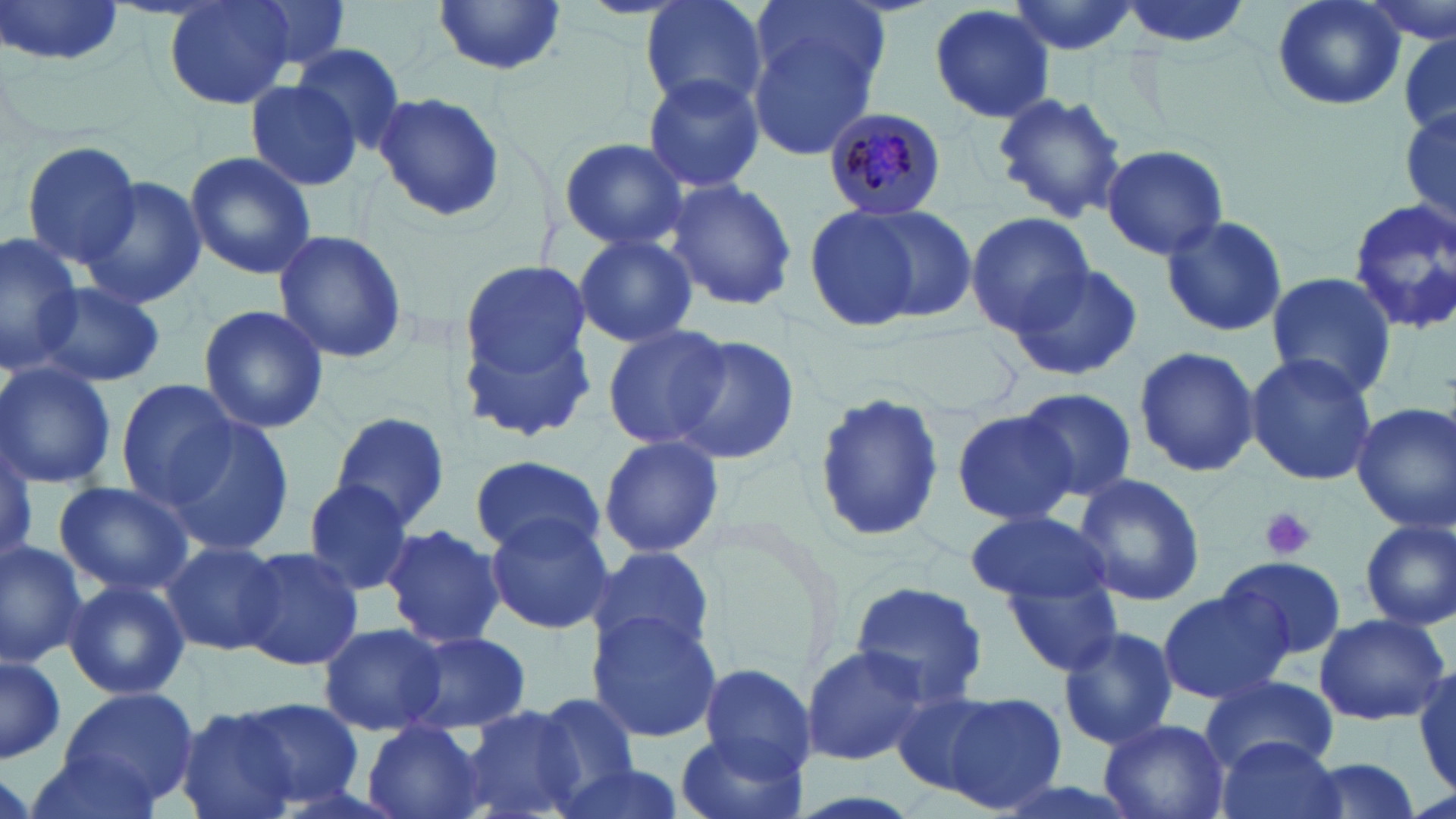
Plasmodium malariae-infected red blood cell locations = approximate bounding boxes as (x1,y1)-(x2,y2) corner pairs in pixels: (821,104)-(951,215)
slide-level diagnosis = Plasmodium malariae
stain = May-Grünwald-Giemsa
platelet locations = approximate bounding boxes as (x1,y1)-(x2,y2) corner pairs in pixels: (1257,506)-(1318,561)
magnification = 1000x
modality = optical microscopy
preparation = thin blood film
uninfected red blood cell locations = approximate bounding boxes as (x1,y1)-(x2,y2) corner pairs in pixels: (162,0)-(295,110), (241,0)-(353,74), (639,0)-(769,115), (751,0)-(893,95), (1003,0)-(1140,57), (1113,0)-(1255,52), (1271,0)-(1405,112), (1362,0)-(1456,47), (1,1)-(127,69), (432,2)-(568,77), (927,4)-(1057,125), (743,20)-(883,162), (1399,38)-(1455,136), (287,43)-(407,152), (641,71)-(766,194), (242,79)-(363,191), (990,90)-(1128,224), (371,92)-(506,222), (1400,96)-(1454,241), (556,137)-(692,253), (19,139)-(145,268), (1100,144)-(1229,260), (183,151)-(316,279), (79,176)-(208,308), (661,177)-(798,311), (1347,199)-(1456,335), (802,203)-(931,335), (846,204)-(978,322), (964,211)-(1096,339), (1160,214)-(1287,338), (272,230)-(409,364), (0,232)-(79,369), (573,233)-(700,348), (457,261)-(597,434), (1006,263)-(1143,383), (1265,271)-(1395,401), (33,282)-(168,387), (196,304)-(331,433), (605,323)-(734,452), (669,335)-(801,466), (1132,345)-(1260,477), (1244,352)-(1377,486), (0,361)-(118,490), (113,378)-(237,505), (1017,388)-(1136,500), (812,390)-(945,547), (1351,402)-(1456,532), (949,409)-(1077,528), (330,411)-(450,530), (163,415)-(295,555), (598,435)-(725,559), (470,454)-(605,558), (1071,473)-(1206,607), (298,479)-(415,594), (53,481)-(196,597), (964,510)-(1109,603), (482,513)-(616,634), (1359,519)-(1455,631), (380,523)-(506,648), (0,538)-(89,665), (159,540)-(287,657), (237,546)-(365,671), (585,546)-(717,661), (1217,555)-(1347,663), (1182,561)-(1337,738), (1002,568)-(1128,677), (63,578)-(189,701), (850,579)-(992,710), (1157,591)-(1290,705), (588,612)-(725,742), (1315,612)-(1451,726), (318,623)-(446,736), (1056,625)-(1177,750), (399,629)-(531,735), (802,644)-(930,767), (0,657)-(64,762), (700,663)-(814,774), (1410,666)-(1456,789), (1202,672)-(1340,773), (60,688)-(198,805), (891,688)-(1002,795), (514,691)-(646,810), (939,692)-(1070,812), (232,697)-(367,810), (458,704)-(593,819), (175,706)-(301,819), (1097,718)-(1228,819), (363,720)-(487,819), (675,731)-(806,819), (1217,736)-(1346,819), (22,744)-(165,818), (1304,759)-(1424,819), (548,762)-(689,819), (983,777)-(1149,819)
image size = 1456×819 pixels
field of view = single